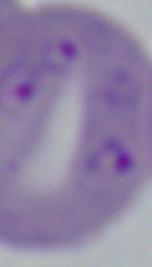

Summary:
  - Identification: Babesia
  - Magnification: 1000x
  - Modality: photomicrograph